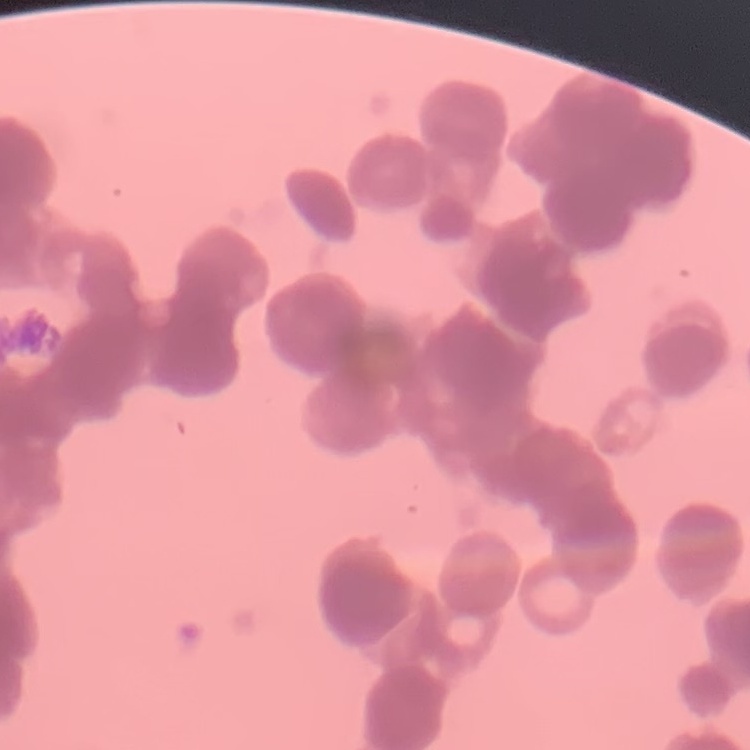

Summary:
  - Red blood cell morphology: rouleaux formation
  - Image type: square crop of a larger photomicrograph
  - Stain: Field's or Giemsa
  - Preparation: thin blood smear